Locate and identify every blood parasite.
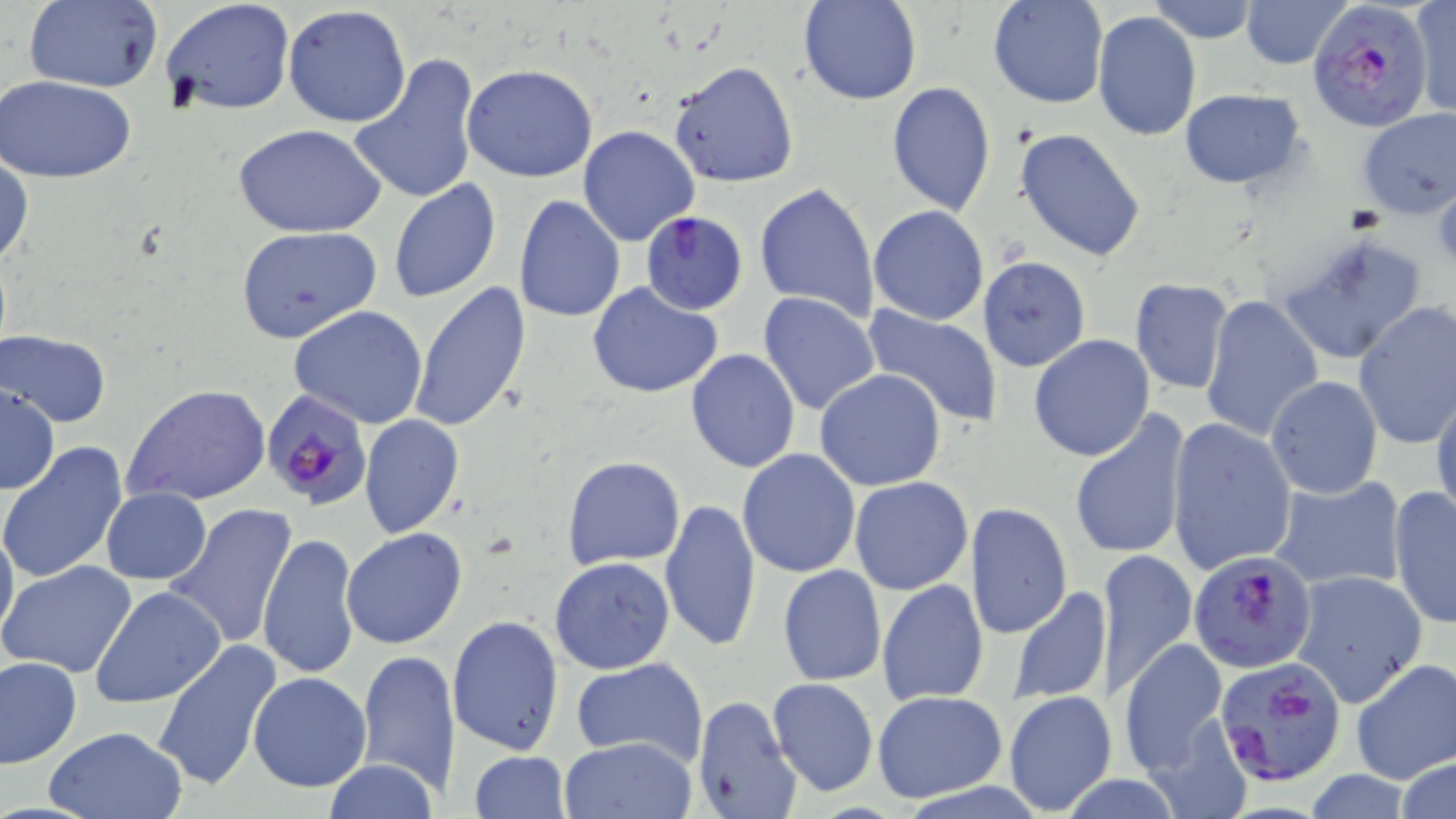
Approximate bounding boxes as named x1/y1/x2/y2 corners in pixels.
Plasmodium falciparum-infected red blood cells: (x1=1309, y1=0, x2=1434, y2=132), (x1=641, y1=210, x2=748, y2=315), (x1=262, y1=391, x2=374, y2=511), (x1=1189, y1=550, x2=1317, y2=675), (x1=1213, y1=653, x2=1349, y2=786).
No Plasmodium ovale, Plasmodium malariae, Plasmodium vivax, Babesia divergens, or Trypanosoma brucei observed.

Uninfected red blood cell locations: (x1=21, y1=0, x2=164, y2=93), (x1=798, y1=0, x2=923, y2=106), (x1=987, y1=0, x2=1108, y2=109), (x1=1148, y1=0, x2=1256, y2=44), (x1=1241, y1=0, x2=1348, y2=69), (x1=1410, y1=0, x2=1456, y2=118), (x1=161, y1=2, x2=294, y2=117), (x1=283, y1=4, x2=412, y2=129), (x1=1093, y1=10, x2=1202, y2=141), (x1=346, y1=52, x2=481, y2=206), (x1=667, y1=60, x2=801, y2=189), (x1=461, y1=63, x2=600, y2=183), (x1=1, y1=75, x2=137, y2=182), (x1=886, y1=80, x2=995, y2=216), (x1=1178, y1=89, x2=1307, y2=189), (x1=1356, y1=107, x2=1456, y2=219), (x1=235, y1=125, x2=384, y2=238), (x1=578, y1=125, x2=702, y2=247), (x1=1013, y1=127, x2=1147, y2=262), (x1=0, y1=154, x2=34, y2=273), (x1=1430, y1=178, x2=1456, y2=268), (x1=387, y1=179, x2=503, y2=303), (x1=755, y1=181, x2=879, y2=324), (x1=512, y1=195, x2=626, y2=323), (x1=868, y1=204, x2=989, y2=325), (x1=236, y1=226, x2=382, y2=343), (x1=1274, y1=230, x2=1430, y2=367), (x1=976, y1=256, x2=1090, y2=374), (x1=1129, y1=278, x2=1234, y2=394), (x1=409, y1=281, x2=533, y2=433), (x1=587, y1=282, x2=726, y2=399), (x1=758, y1=292, x2=881, y2=416), (x1=1201, y1=294, x2=1325, y2=441), (x1=1352, y1=302, x2=1456, y2=449), (x1=287, y1=305, x2=430, y2=429), (x1=858, y1=305, x2=1008, y2=427), (x1=1, y1=329, x2=111, y2=427), (x1=1028, y1=334, x2=1156, y2=462), (x1=686, y1=348, x2=801, y2=472), (x1=813, y1=369, x2=947, y2=493), (x1=1265, y1=376, x2=1382, y2=500), (x1=2, y1=383, x2=61, y2=494), (x1=122, y1=384, x2=271, y2=506), (x1=1431, y1=386, x2=1456, y2=526), (x1=1069, y1=412, x2=1190, y2=562), (x1=359, y1=414, x2=464, y2=538), (x1=1166, y1=419, x2=1298, y2=575), (x1=0, y1=444, x2=128, y2=584), (x1=736, y1=448, x2=862, y2=578), (x1=561, y1=455, x2=687, y2=569), (x1=849, y1=476, x2=973, y2=596), (x1=1267, y1=476, x2=1406, y2=593), (x1=1389, y1=486, x2=1455, y2=629), (x1=100, y1=487, x2=212, y2=585), (x1=660, y1=497, x2=762, y2=653), (x1=165, y1=502, x2=299, y2=654), (x1=965, y1=502, x2=1073, y2=640), (x1=0, y1=515, x2=18, y2=647), (x1=341, y1=527, x2=468, y2=650), (x1=257, y1=531, x2=361, y2=681), (x1=120, y1=546, x2=284, y2=695), (x1=1095, y1=547, x2=1197, y2=700), (x1=549, y1=557, x2=676, y2=674), (x1=0, y1=560, x2=136, y2=678), (x1=777, y1=564, x2=886, y2=686), (x1=1289, y1=570, x2=1428, y2=708), (x1=876, y1=579, x2=989, y2=707), (x1=1007, y1=585, x2=1112, y2=705), (x1=90, y1=586, x2=227, y2=708), (x1=446, y1=615, x2=564, y2=756), (x1=151, y1=637, x2=283, y2=792), (x1=1118, y1=637, x2=1230, y2=777), (x1=356, y1=647, x2=460, y2=797), (x1=1, y1=656, x2=82, y2=768), (x1=572, y1=657, x2=708, y2=769), (x1=1350, y1=658, x2=1456, y2=785), (x1=248, y1=672, x2=372, y2=792), (x1=768, y1=677, x2=879, y2=797), (x1=1003, y1=690, x2=1118, y2=816), (x1=873, y1=691, x2=1006, y2=802), (x1=691, y1=694, x2=802, y2=819), (x1=43, y1=727, x2=187, y2=819), (x1=559, y1=736, x2=697, y2=819), (x1=466, y1=750, x2=572, y2=819), (x1=323, y1=758, x2=437, y2=819). Slide-level diagnosis: Plasmodium falciparum. Single field of view. Light microscopy. Image is 1456×819 pixels. Thin blood film. May-Grünwald-Giemsa stain. Captured at 1000x magnification.